Outline each Plasmodium ovale-infected red blood cell.
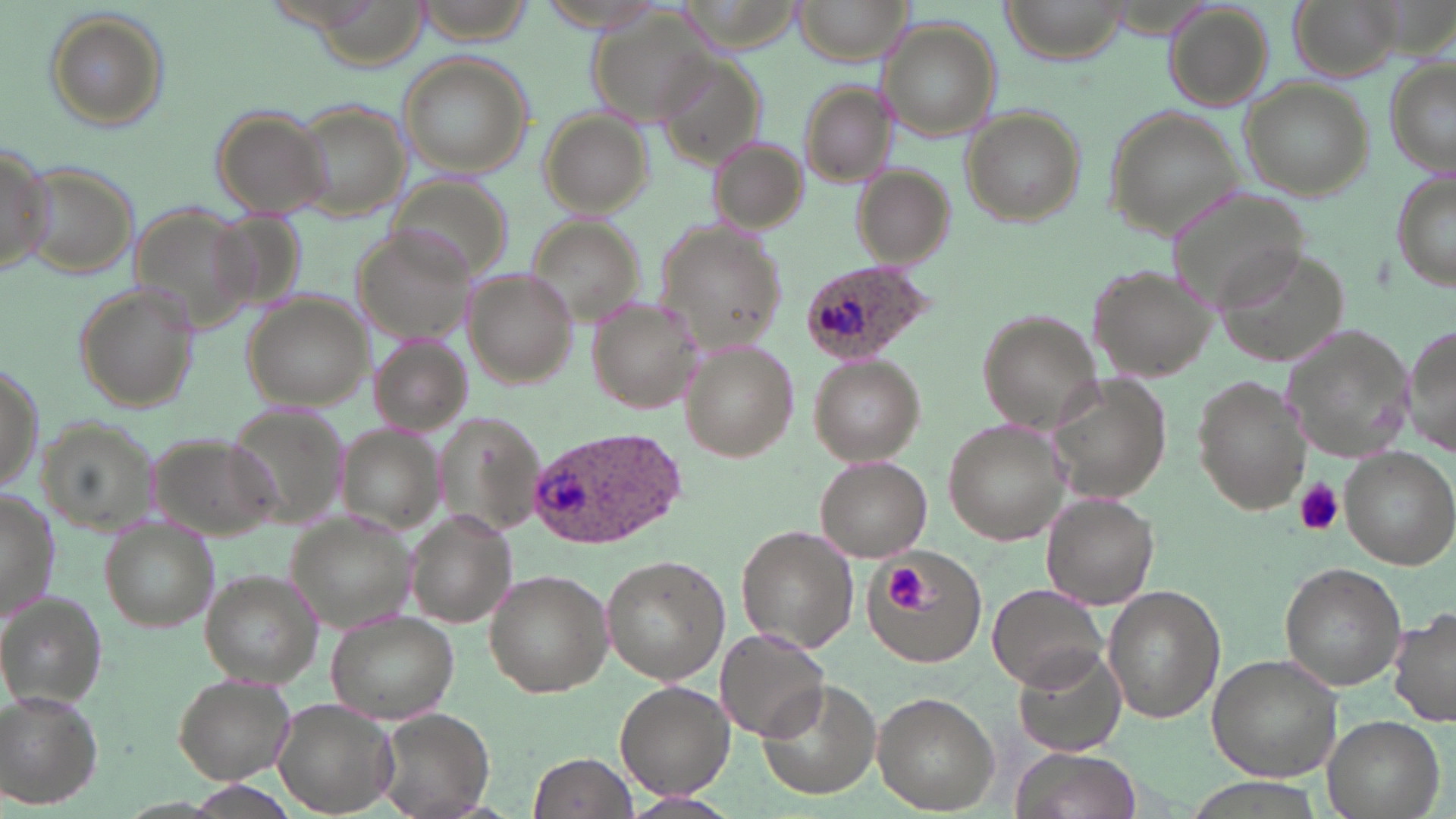
Approximate bounding boxes as (x1, y1, x2, y2) in pixels.
Plasmodium ovale-infected red blood cells: (798, 258, 935, 369), (527, 427, 689, 549).

Summary:
  - Uninfected red blood cell locations: (790, 0, 913, 65), (1001, 0, 1129, 64), (1286, 0, 1408, 82), (590, 1, 721, 131), (307, 3, 432, 77), (1167, 3, 1272, 108), (42, 11, 171, 134), (880, 20, 999, 137), (650, 50, 768, 169), (394, 52, 534, 178), (1381, 58, 1456, 180), (796, 79, 903, 188), (1241, 80, 1371, 202), (289, 104, 410, 220), (208, 106, 333, 220), (961, 107, 1086, 227), (538, 108, 652, 218), (1105, 108, 1248, 240), (704, 134, 807, 233), (0, 139, 53, 276), (17, 160, 140, 280), (852, 167, 953, 268), (1391, 168, 1455, 293), (389, 169, 514, 289), (1167, 188, 1311, 314), (126, 199, 264, 336), (209, 207, 308, 315), (526, 211, 648, 330), (654, 223, 786, 352), (352, 224, 481, 348), (1217, 247, 1348, 367), (1087, 263, 1221, 384), (462, 266, 580, 390), (73, 282, 194, 411), (240, 292, 372, 408), (585, 297, 701, 413), (976, 309, 1103, 433), (1280, 324, 1416, 464), (1402, 324, 1456, 452), (366, 333, 472, 437), (679, 338, 799, 463), (810, 355, 924, 464), (1042, 373, 1177, 501), (1192, 375, 1311, 515), (228, 402, 346, 531), (434, 415, 547, 540), (37, 416, 163, 531), (942, 420, 1066, 544), (335, 423, 452, 538), (143, 433, 284, 545), (1339, 448, 1454, 569), (816, 456, 931, 561), (0, 492, 57, 626), (1040, 493, 1161, 609), (285, 508, 423, 633), (405, 509, 518, 627), (101, 519, 217, 632), (736, 524, 858, 655), (864, 548, 986, 665), (600, 554, 729, 683), (1279, 562, 1406, 691), (199, 567, 325, 686), (484, 570, 614, 696), (988, 583, 1111, 691), (1102, 584, 1226, 724), (1, 594, 107, 708), (1389, 606, 1456, 727), (325, 610, 463, 725), (717, 626, 830, 743), (1013, 645, 1129, 758), (1207, 654, 1344, 780), (171, 673, 295, 784), (758, 678, 881, 802), (615, 681, 734, 799), (873, 690, 1001, 814), (0, 691, 101, 808), (269, 698, 401, 819), (370, 708, 494, 819), (1320, 715, 1443, 819), (1014, 750, 1137, 819), (528, 753, 637, 818), (628, 791, 735, 817)
  - Platelet locations: (1292, 478, 1345, 536), (887, 565, 942, 617)
  - Slide-level diagnosis: Plasmodium ovale
  - Field of view: single
  - Image size: 1456×819 pixels
  - Magnification: 1000x
  - Stain: May-Grünwald-Giemsa
  - Modality: light microscopy
  - Preparation: thin blood film